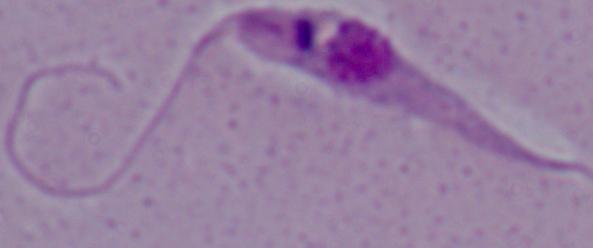
modality = micrograph
magnification = 1000x
identification = Leishmania